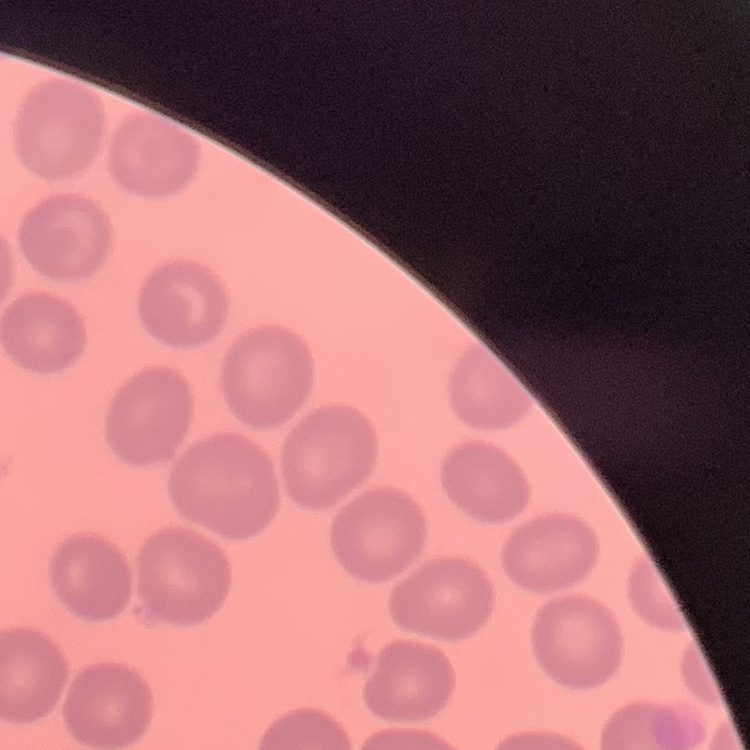
Summary:
  - Red blood cell morphology: no rouleaux formation
  - Preparation: thin blood film
  - Stain: Field's or Giemsa
  - Image type: one tile cut from a larger photomicrograph